Report the malaria status of this cell.
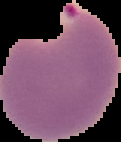
Parasitized.

image size = 121×142 pixels
preparation = thin blood film
image type = segmented cell region on a black background